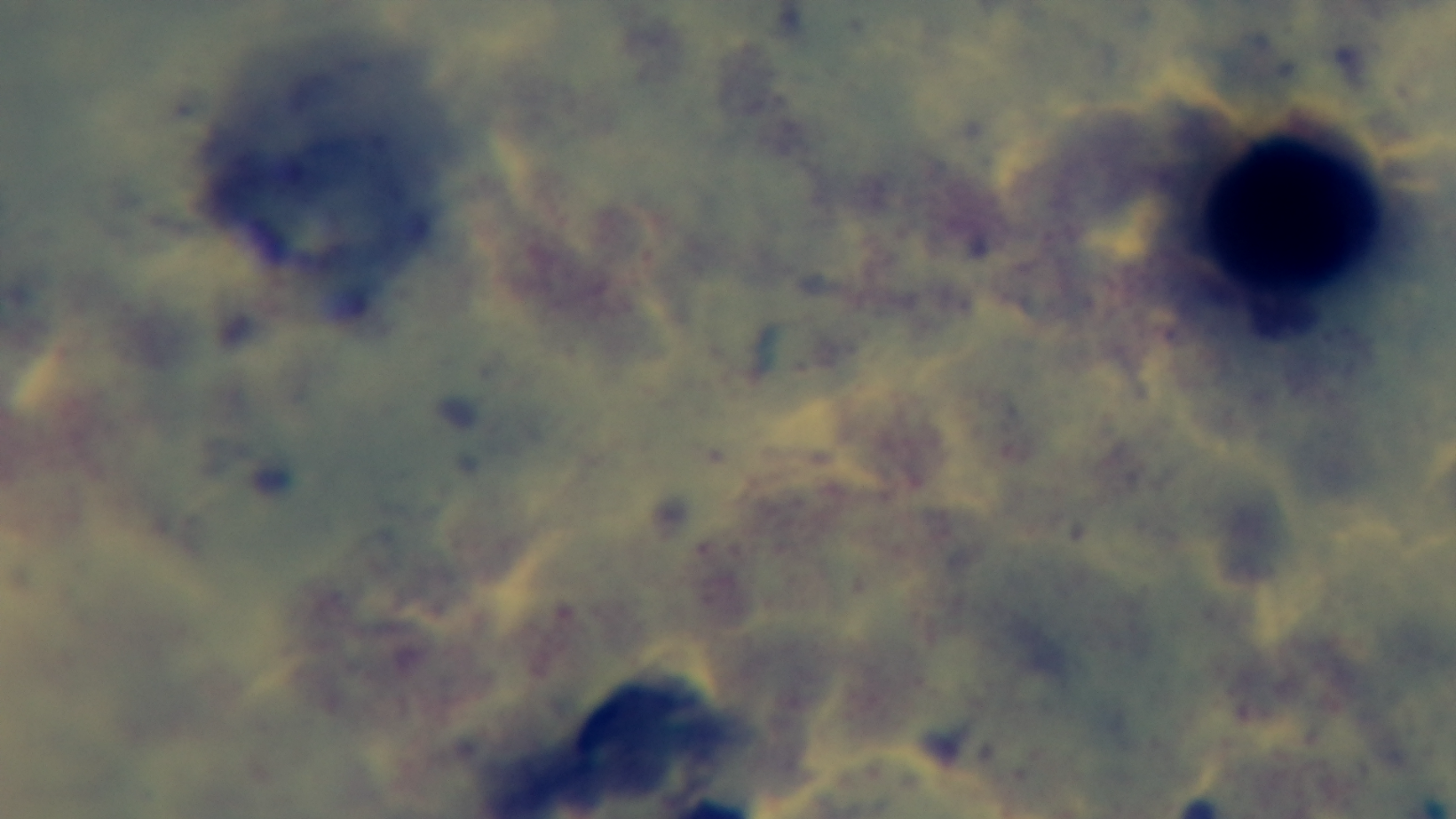
malaria status = negative
objective = 100x oil immersion
modality = light microscopy
stain = Giemsa
capture = mounted 4K digital camera
field of view = one from the slide
preparation = thick blood film